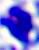

Photomicrograph. A leukocyte is seen. Captured at 400x magnification.